Assess the morphology of the erythrocytes.
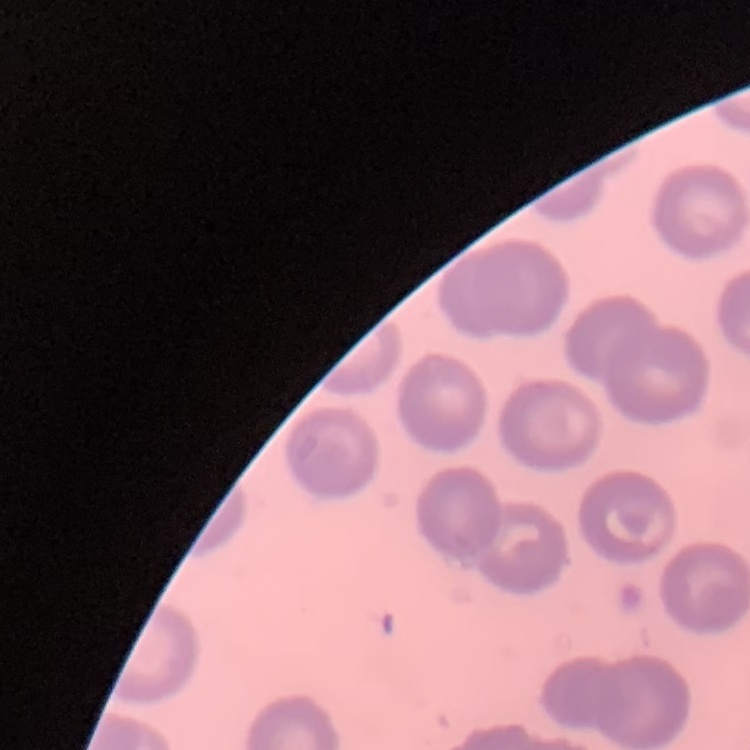

They show no rouleaux formation.

Square crop of a larger photomicrograph. Stained with either Field's or Giemsa. Thin blood film.